Classify this cell by malaria status.
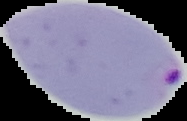
Parasitized.

image size = 187×121 pixels
image type = cell region segmented out of the field of view; surrounding area masked to black
preparation = thin blood film